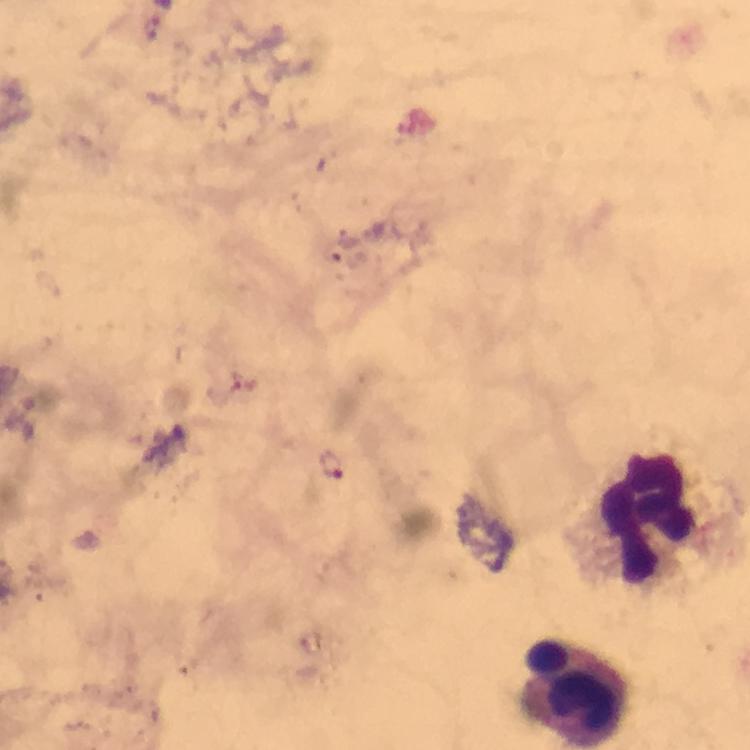
Approximate centers as [x, y] in pixels. Leukocyte locations: [646, 514], [578, 692]. Malaria parasite locations: [334, 462]. Thick blood smear. Photographed with a smartphone mounted on the microscope. Giemsa-stained preparation. From a diagnostic examination for malaria. Image is 750×750 pixels. Immersion oil applied. Cropped region of a single field of view. At 100x magnification.